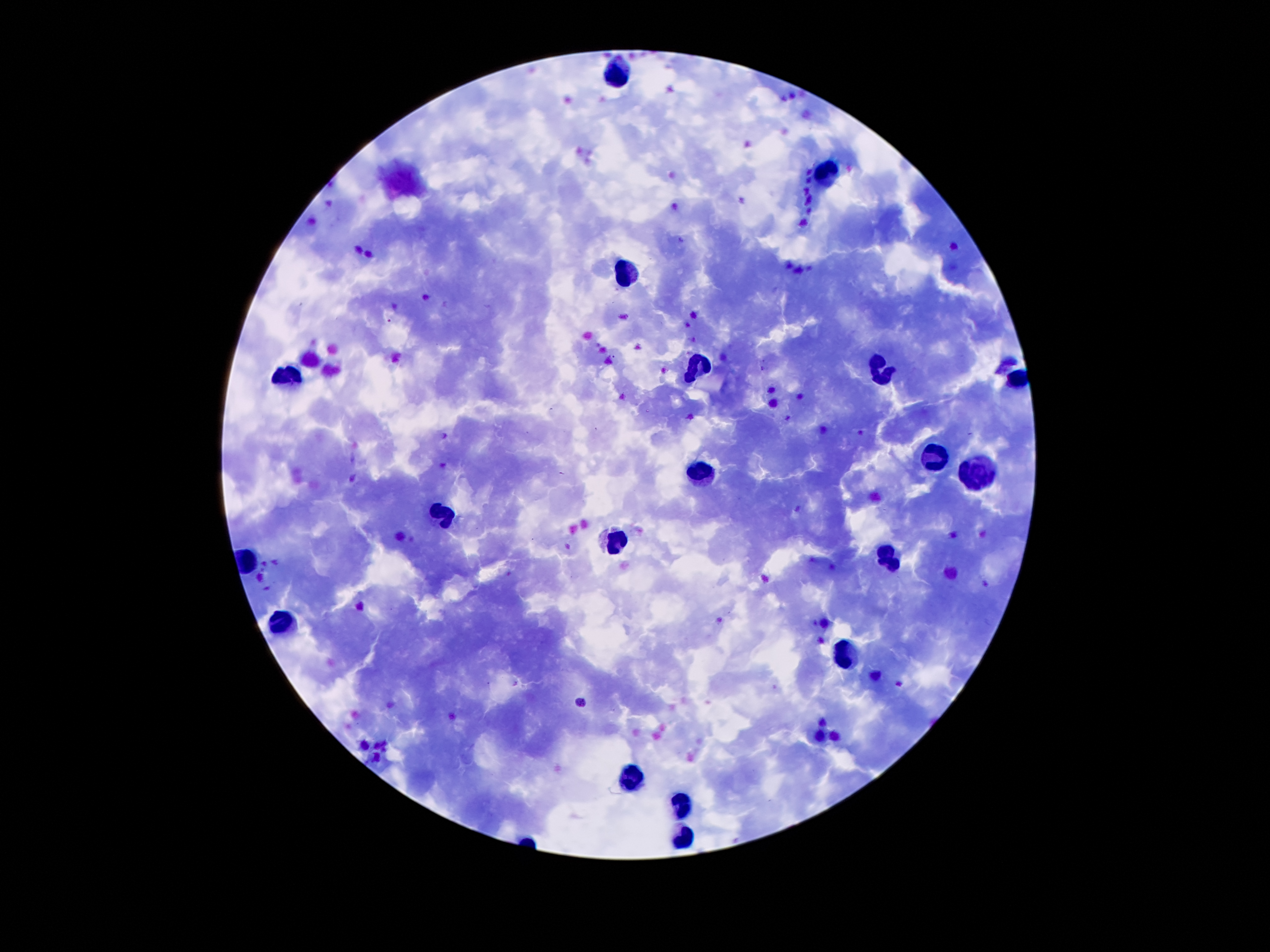 100x magnification. Giemsa-stained preparation. Thick blood smear. Image is 1270×952 pixels. One field from this slide. Patient malaria status: infected with Plasmodium falciparum. Smartphone photograph taken through the microscope eyepiece.